Identify the cell.
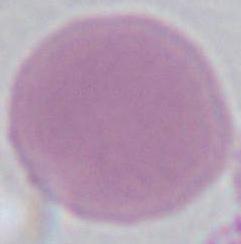

This is an erythrocyte.

1000x magnification. Micrograph.